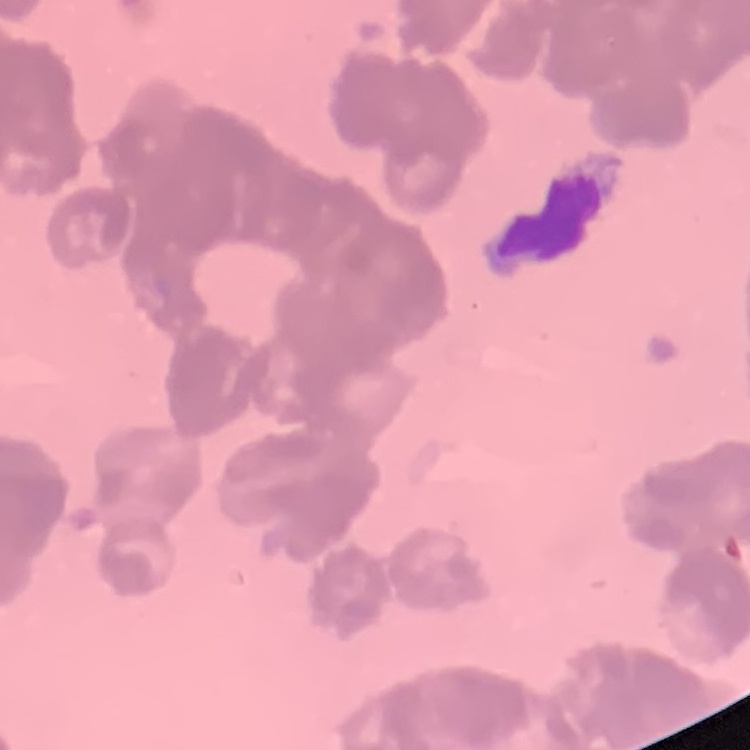
erythrocyte morphology = rouleaux formation
preparation = thin blood smear
image type = square crop of a larger photomicrograph
stain = Field's or Giemsa